Locate every uninfected red blood cell.
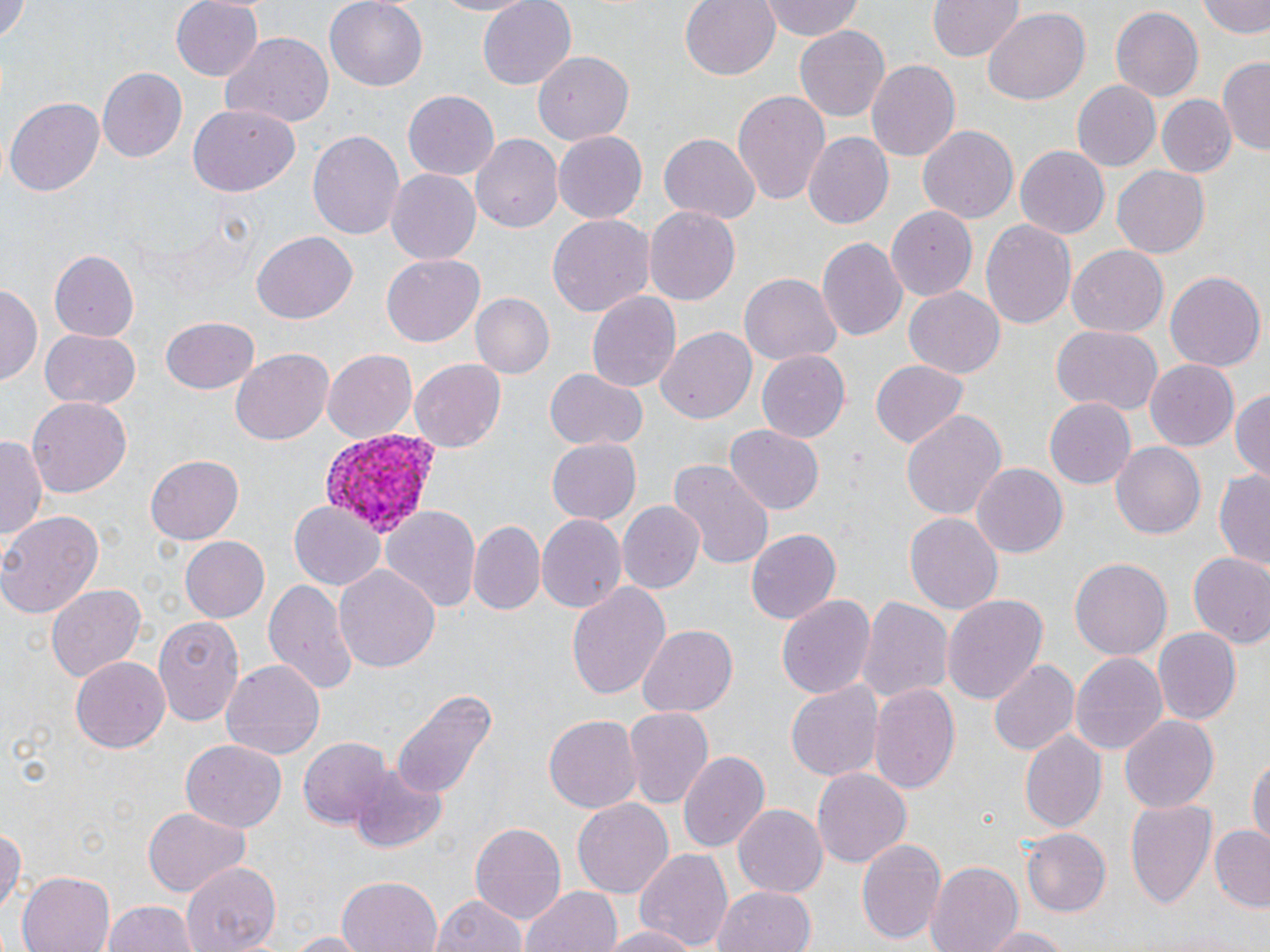
Approximate bounding boxes as named x1/y1/x2/y2 corners in pixels.
Uninfected red blood cells: (x1=0, y1=0, x2=29, y2=51), (x1=169, y1=0, x2=263, y2=80), (x1=324, y1=0, x2=428, y2=92), (x1=422, y1=0, x2=542, y2=17), (x1=477, y1=0, x2=577, y2=89), (x1=678, y1=0, x2=782, y2=81), (x1=757, y1=0, x2=867, y2=45), (x1=1200, y1=0, x2=1270, y2=39), (x1=929, y1=1, x2=1022, y2=62), (x1=1110, y1=6, x2=1202, y2=102), (x1=982, y1=8, x2=1090, y2=105), (x1=795, y1=24, x2=891, y2=121), (x1=219, y1=32, x2=334, y2=127), (x1=535, y1=51, x2=634, y2=145), (x1=866, y1=57, x2=959, y2=159), (x1=1219, y1=57, x2=1270, y2=156), (x1=97, y1=67, x2=186, y2=162), (x1=1071, y1=80, x2=1162, y2=172), (x1=733, y1=90, x2=830, y2=205), (x1=402, y1=91, x2=499, y2=182), (x1=6, y1=95, x2=106, y2=196), (x1=1157, y1=96, x2=1235, y2=177), (x1=189, y1=104, x2=299, y2=196), (x1=917, y1=125, x2=1018, y2=223), (x1=308, y1=130, x2=405, y2=245), (x1=802, y1=130, x2=893, y2=228), (x1=553, y1=132, x2=646, y2=222), (x1=659, y1=132, x2=759, y2=222), (x1=470, y1=134, x2=561, y2=236), (x1=1015, y1=145, x2=1109, y2=238), (x1=1113, y1=164, x2=1210, y2=257), (x1=387, y1=170, x2=481, y2=264), (x1=643, y1=204, x2=739, y2=304), (x1=885, y1=205, x2=976, y2=299), (x1=546, y1=214, x2=654, y2=320), (x1=979, y1=218, x2=1076, y2=332), (x1=252, y1=231, x2=357, y2=323), (x1=817, y1=236, x2=907, y2=340), (x1=1067, y1=246, x2=1168, y2=338), (x1=49, y1=249, x2=138, y2=343), (x1=382, y1=256, x2=484, y2=345), (x1=1166, y1=270, x2=1265, y2=371), (x1=740, y1=272, x2=841, y2=365), (x1=0, y1=281, x2=42, y2=384), (x1=905, y1=287, x2=1005, y2=378), (x1=586, y1=290, x2=682, y2=394), (x1=471, y1=292, x2=555, y2=378), (x1=161, y1=317, x2=260, y2=394), (x1=1050, y1=326, x2=1163, y2=415), (x1=656, y1=327, x2=755, y2=427), (x1=39, y1=330, x2=141, y2=410), (x1=232, y1=347, x2=333, y2=445), (x1=322, y1=347, x2=418, y2=441), (x1=755, y1=348, x2=849, y2=441), (x1=409, y1=359, x2=506, y2=453), (x1=868, y1=359, x2=969, y2=450), (x1=1146, y1=360, x2=1239, y2=448), (x1=544, y1=368, x2=648, y2=453), (x1=1232, y1=388, x2=1270, y2=479), (x1=29, y1=398, x2=133, y2=497), (x1=1045, y1=398, x2=1135, y2=489), (x1=900, y1=410, x2=1007, y2=520), (x1=725, y1=424, x2=824, y2=515), (x1=1, y1=433, x2=45, y2=549), (x1=548, y1=440, x2=640, y2=524), (x1=1111, y1=444, x2=1204, y2=537), (x1=146, y1=453, x2=243, y2=544), (x1=668, y1=459, x2=774, y2=571), (x1=971, y1=463, x2=1068, y2=558), (x1=1215, y1=468, x2=1270, y2=574), (x1=616, y1=500, x2=706, y2=595), (x1=289, y1=503, x2=384, y2=590), (x1=383, y1=507, x2=479, y2=611), (x1=0, y1=508, x2=104, y2=618), (x1=904, y1=511, x2=1007, y2=614), (x1=536, y1=516, x2=624, y2=615), (x1=468, y1=520, x2=545, y2=615), (x1=746, y1=528, x2=839, y2=624), (x1=182, y1=537, x2=271, y2=623), (x1=1186, y1=552, x2=1270, y2=648), (x1=1069, y1=557, x2=1171, y2=662), (x1=332, y1=562, x2=439, y2=670), (x1=264, y1=578, x2=359, y2=693), (x1=567, y1=580, x2=671, y2=700), (x1=45, y1=583, x2=146, y2=681), (x1=775, y1=592, x2=877, y2=700), (x1=859, y1=594, x2=953, y2=704), (x1=942, y1=594, x2=1049, y2=705), (x1=154, y1=614, x2=245, y2=727), (x1=639, y1=626, x2=737, y2=717), (x1=1153, y1=628, x2=1242, y2=727), (x1=1071, y1=651, x2=1168, y2=757), (x1=71, y1=656, x2=170, y2=754), (x1=989, y1=659, x2=1079, y2=757), (x1=223, y1=660, x2=324, y2=761), (x1=787, y1=677, x2=882, y2=783), (x1=868, y1=682, x2=961, y2=797), (x1=388, y1=688, x2=498, y2=802), (x1=622, y1=705, x2=713, y2=807), (x1=1120, y1=713, x2=1218, y2=812), (x1=544, y1=714, x2=642, y2=813), (x1=1021, y1=731, x2=1106, y2=834), (x1=298, y1=735, x2=392, y2=831), (x1=181, y1=740, x2=286, y2=832), (x1=677, y1=749, x2=770, y2=855), (x1=1248, y1=754, x2=1270, y2=856), (x1=347, y1=766, x2=446, y2=853), (x1=813, y1=768, x2=911, y2=870), (x1=572, y1=796, x2=672, y2=900), (x1=1123, y1=799, x2=1217, y2=913), (x1=734, y1=804, x2=826, y2=899), (x1=142, y1=806, x2=248, y2=897), (x1=468, y1=820, x2=565, y2=924), (x1=0, y1=824, x2=23, y2=914), (x1=1210, y1=824, x2=1270, y2=911), (x1=1023, y1=829, x2=1112, y2=916), (x1=856, y1=837, x2=945, y2=946), (x1=635, y1=848, x2=732, y2=949), (x1=182, y1=861, x2=279, y2=950), (x1=930, y1=861, x2=1026, y2=952), (x1=17, y1=872, x2=114, y2=952), (x1=338, y1=875, x2=441, y2=952), (x1=713, y1=887, x2=822, y2=952), (x1=523, y1=888, x2=625, y2=952), (x1=433, y1=893, x2=529, y2=952), (x1=101, y1=899, x2=195, y2=952), (x1=598, y1=925, x2=704, y2=952), (x1=976, y1=926, x2=1077, y2=951), (x1=276, y1=930, x2=377, y2=950).

Plasmodium vivax-infected red blood cell locations: (x1=316, y1=429, x2=443, y2=539). Slide-level diagnosis: Plasmodium vivax. One field of a larger specimen. Light microscopy. May-Grünwald-Giemsa-stained preparation. Thin blood film. 1000x magnification. Image is 1270×952 pixels.